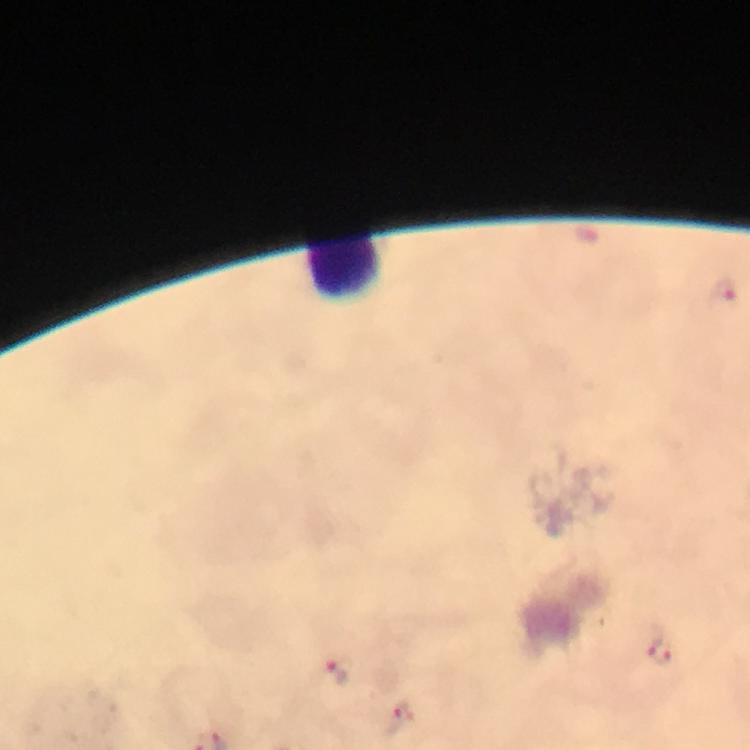

Approximate centers as [x, y] in pixels.
Summary:
  - Plasmodium parasite locations: [585, 235], [722, 296], [657, 650], [333, 673], [398, 717]
  - Leukocyte locations: [345, 265]
  - Context: from a malaria diagnostic workup
  - Immersion oil: used
  - Image size: 750×750 pixels
  - Magnification: 100x
  - Stain: Giemsa
  - Preparation: thick smear
  - Cropped from: a single field of view
  - Capture: smartphone camera through the microscope